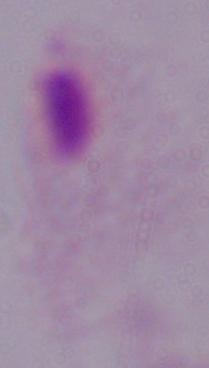 1000x magnification. Photomicrograph. A trichomonad is shown.